Locate every Plasmodium parasite.
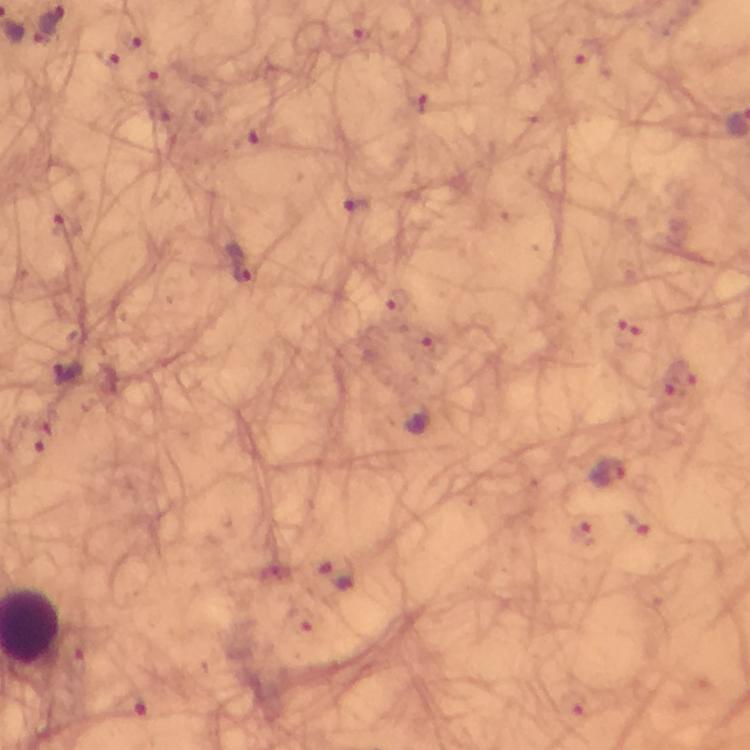
Approximate object centers, in pixels from the top-left corner.
Plasmodium parasites: (x=356, y=209), (x=68, y=227), (x=238, y=264), (x=68, y=373), (x=45, y=436), (x=608, y=472), (x=340, y=572), (x=131, y=706).

Summary:
  - Magnification: 100x
  - Context: from a malaria diagnostic workup
  - Cropped from: one field of view
  - Immersion oil: used
  - Stain: Giemsa
  - Preparation: thick blood smear
  - Capture: smartphone photograph through a microscope
  - Image size: 750×750 pixels